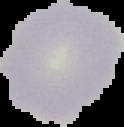
{
  "image_size": "124×127 pixels",
  "malaria_status": "uninfected",
  "image_type": "segmented cell region on a black background",
  "preparation": "thin blood film"
}